Assess this cell for malaria.
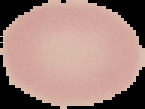
Uninfected.

From a thin blood film. Image is 145×109 pixels. The area outside the segmented cell region is set to black.